Outline each blood parasite and name the species.
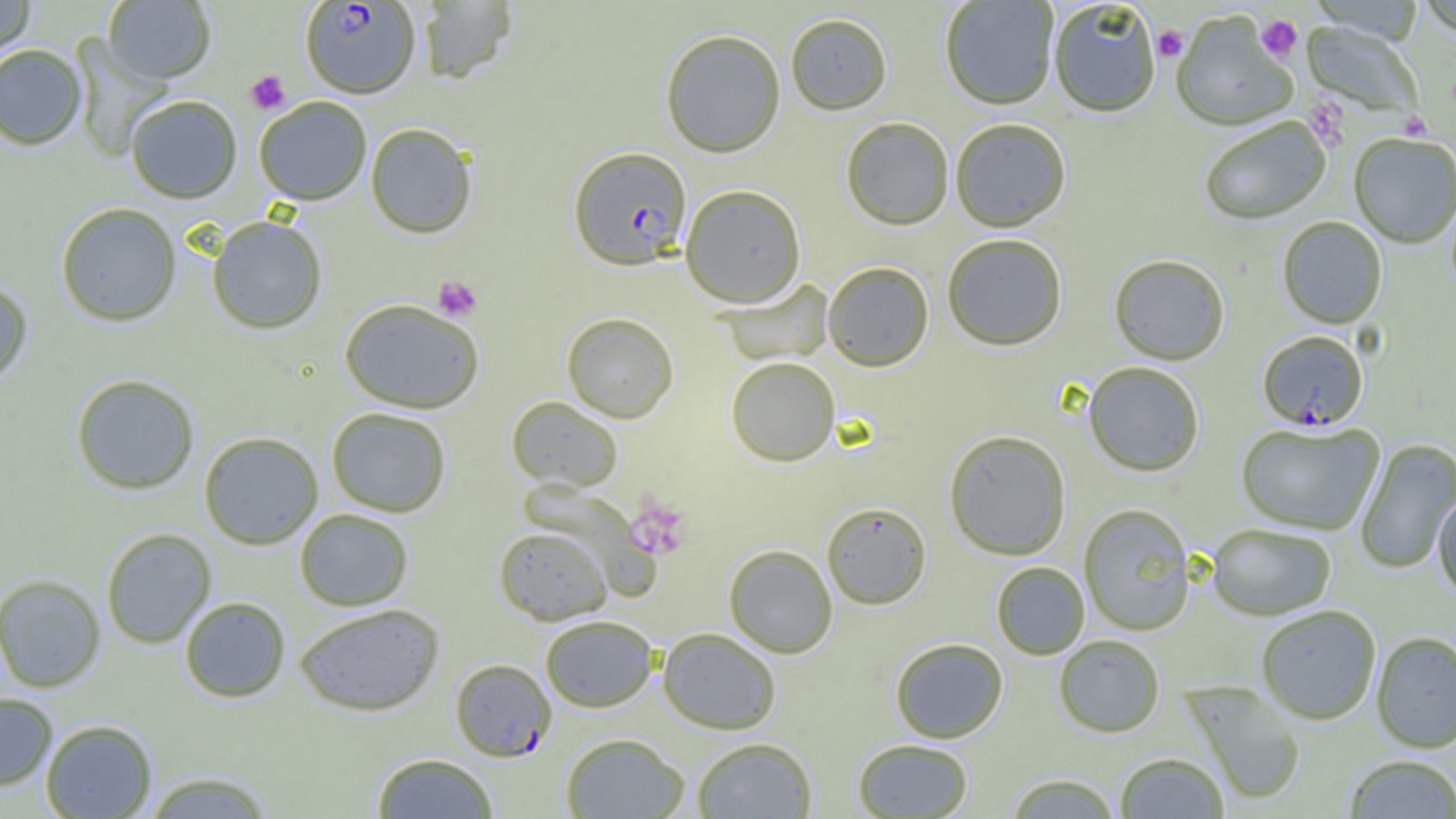

Approximate bounding boxes as named x1/y1/x2/y2 corners in pixels.
Plasmodium falciparum-infected red blood cells: (x1=300, y1=1, x2=421, y2=99), (x1=569, y1=147, x2=692, y2=270), (x1=1257, y1=332, x2=1368, y2=433), (x1=450, y1=659, x2=556, y2=761).
No Plasmodium ovale, Plasmodium malariae, Plasmodium vivax, Babesia divergens, or Trypanosoma brucei observed.

{
  "slide_level_diagnosis": "Plasmodium falciparum",
  "uninfected_red_blood_cell_locations": "approximate bounding boxes as named x1/y1/x2/y2 corners in pixels: (x1=0, y1=0, x2=35, y2=60), (x1=103, y1=0, x2=216, y2=84), (x1=940, y1=0, x2=1059, y2=112), (x1=416, y1=1, x2=518, y2=84), (x1=1416, y1=2, x2=1456, y2=42), (x1=1049, y1=3, x2=1160, y2=119), (x1=1171, y1=12, x2=1297, y2=134), (x1=785, y1=14, x2=892, y2=116), (x1=1301, y1=21, x2=1424, y2=121), (x1=659, y1=29, x2=786, y2=158), (x1=70, y1=38, x2=174, y2=160), (x1=0, y1=45, x2=86, y2=151), (x1=125, y1=95, x2=242, y2=204), (x1=253, y1=97, x2=372, y2=205), (x1=841, y1=118, x2=954, y2=231), (x1=1200, y1=118, x2=1331, y2=227), (x1=950, y1=119, x2=1071, y2=234), (x1=365, y1=123, x2=478, y2=239), (x1=1349, y1=135, x2=1456, y2=249), (x1=680, y1=184, x2=806, y2=308), (x1=55, y1=203, x2=182, y2=327), (x1=206, y1=216, x2=328, y2=335), (x1=1278, y1=217, x2=1387, y2=330), (x1=942, y1=235, x2=1067, y2=352), (x1=1109, y1=256, x2=1229, y2=367), (x1=823, y1=262, x2=934, y2=372), (x1=0, y1=278, x2=34, y2=389), (x1=717, y1=279, x2=834, y2=366), (x1=339, y1=298, x2=485, y2=414), (x1=562, y1=312, x2=679, y2=423), (x1=725, y1=357, x2=840, y2=467), (x1=1084, y1=364, x2=1204, y2=478), (x1=70, y1=373, x2=200, y2=496), (x1=506, y1=396, x2=623, y2=492), (x1=326, y1=407, x2=452, y2=517), (x1=1236, y1=422, x2=1385, y2=536), (x1=944, y1=430, x2=1071, y2=561), (x1=198, y1=431, x2=324, y2=550), (x1=1355, y1=439, x2=1456, y2=574), (x1=1433, y1=494, x2=1456, y2=604), (x1=821, y1=503, x2=932, y2=610), (x1=1078, y1=504, x2=1195, y2=637), (x1=294, y1=508, x2=414, y2=611), (x1=1207, y1=524, x2=1336, y2=622), (x1=493, y1=526, x2=612, y2=625), (x1=100, y1=528, x2=217, y2=649), (x1=723, y1=544, x2=838, y2=658), (x1=991, y1=562, x2=1089, y2=660), (x1=0, y1=574, x2=105, y2=693), (x1=179, y1=596, x2=291, y2=703), (x1=294, y1=603, x2=444, y2=717), (x1=1255, y1=606, x2=1381, y2=725), (x1=540, y1=615, x2=658, y2=712), (x1=658, y1=627, x2=781, y2=735), (x1=1371, y1=631, x2=1456, y2=754), (x1=1053, y1=635, x2=1165, y2=738), (x1=890, y1=638, x2=1008, y2=744), (x1=1181, y1=681, x2=1306, y2=806), (x1=0, y1=693, x2=58, y2=791), (x1=40, y1=719, x2=157, y2=818), (x1=561, y1=732, x2=690, y2=819), (x1=691, y1=737, x2=817, y2=818), (x1=853, y1=739, x2=973, y2=818), (x1=371, y1=752, x2=499, y2=818), (x1=1115, y1=753, x2=1229, y2=818), (x1=1344, y1=755, x2=1456, y2=818), (x1=141, y1=770, x2=276, y2=818), (x1=1004, y1=773, x2=1122, y2=818)",
  "platelet_locations": "approximate bounding boxes as named x1/y1/x2/y2 corners in pixels: (x1=1255, y1=14, x2=1303, y2=64), (x1=1152, y1=25, x2=1188, y2=63), (x1=245, y1=70, x2=291, y2=114), (x1=1303, y1=98, x2=1350, y2=152), (x1=1400, y1=112, x2=1432, y2=140), (x1=432, y1=275, x2=482, y2=322), (x1=627, y1=498, x2=692, y2=560)",
  "preparation": "thin blood film",
  "magnification": "1000x",
  "image_size": "1456×819 pixels",
  "field_of_view": "one of a larger specimen",
  "modality": "light microscopy"
}